Locate and identify every blood parasite.
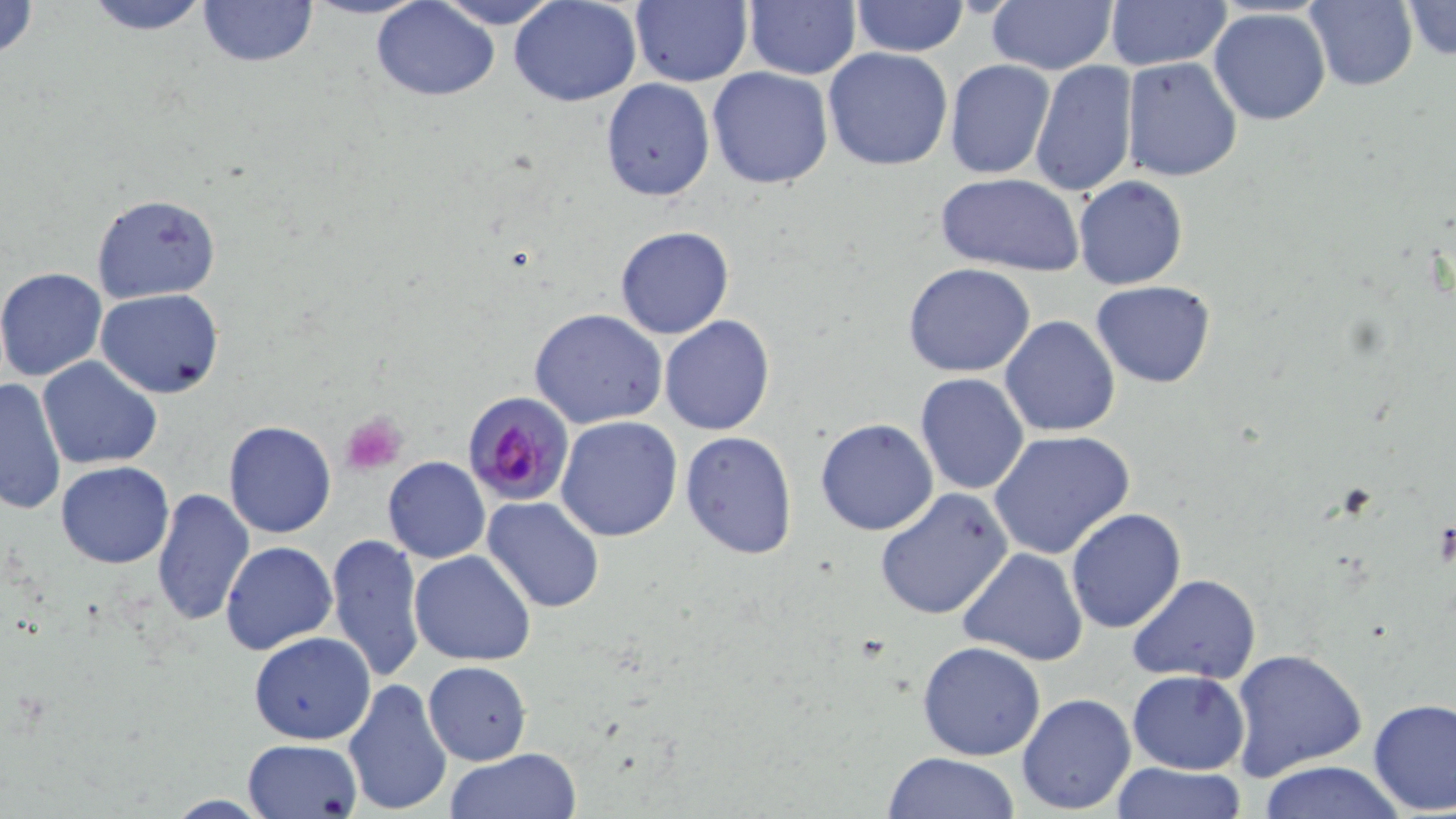

Approximate bounding boxes as named x1/y1/x2/y2 corners in pixels.
Plasmodium falciparum-infected red blood cells: (x1=464, y1=393, x2=576, y2=507).
No Plasmodium ovale, Plasmodium malariae, Plasmodium vivax, Babesia divergens, or Trypanosoma brucei observed.

Platelet locations: (x1=340, y1=411, x2=409, y2=474). Uninfected red blood cell locations: (x1=0, y1=0, x2=41, y2=65), (x1=80, y1=0, x2=215, y2=35), (x1=198, y1=0, x2=317, y2=67), (x1=302, y1=0, x2=428, y2=19), (x1=431, y1=0, x2=567, y2=29), (x1=508, y1=0, x2=643, y2=106), (x1=629, y1=0, x2=753, y2=87), (x1=743, y1=0, x2=861, y2=80), (x1=984, y1=0, x2=1119, y2=74), (x1=1302, y1=0, x2=1418, y2=91), (x1=1399, y1=0, x2=1455, y2=63), (x1=370, y1=1, x2=502, y2=101), (x1=850, y1=1, x2=969, y2=56), (x1=1103, y1=1, x2=1233, y2=71), (x1=1207, y1=8, x2=1332, y2=126), (x1=1138, y1=32, x2=1305, y2=169), (x1=823, y1=46, x2=953, y2=172), (x1=1120, y1=56, x2=1242, y2=181), (x1=945, y1=59, x2=1055, y2=179), (x1=1031, y1=61, x2=1138, y2=197), (x1=706, y1=66, x2=834, y2=190), (x1=600, y1=78, x2=716, y2=201), (x1=934, y1=173, x2=1085, y2=275), (x1=1074, y1=175, x2=1188, y2=291), (x1=90, y1=192, x2=221, y2=306), (x1=614, y1=225, x2=735, y2=341), (x1=901, y1=262, x2=1038, y2=378), (x1=0, y1=267, x2=109, y2=382), (x1=1092, y1=280, x2=1215, y2=387), (x1=95, y1=289, x2=224, y2=398), (x1=530, y1=309, x2=668, y2=429), (x1=659, y1=315, x2=775, y2=437), (x1=1000, y1=315, x2=1121, y2=438), (x1=37, y1=357, x2=163, y2=472), (x1=914, y1=372, x2=1029, y2=496), (x1=0, y1=376, x2=69, y2=515), (x1=555, y1=415, x2=684, y2=542), (x1=814, y1=419, x2=940, y2=536), (x1=223, y1=420, x2=336, y2=538), (x1=988, y1=429, x2=1134, y2=560), (x1=679, y1=431, x2=798, y2=559), (x1=383, y1=456, x2=489, y2=563), (x1=57, y1=461, x2=174, y2=567), (x1=876, y1=487, x2=1013, y2=621), (x1=152, y1=488, x2=255, y2=627), (x1=480, y1=495, x2=606, y2=615), (x1=1064, y1=506, x2=1186, y2=633), (x1=326, y1=533, x2=426, y2=684), (x1=220, y1=540, x2=338, y2=654), (x1=958, y1=547, x2=1089, y2=666), (x1=408, y1=549, x2=536, y2=666), (x1=1127, y1=574, x2=1261, y2=685), (x1=250, y1=631, x2=376, y2=744), (x1=293, y1=638, x2=436, y2=779), (x1=917, y1=639, x2=1046, y2=761), (x1=1229, y1=646, x2=1366, y2=777), (x1=424, y1=661, x2=531, y2=765), (x1=1127, y1=670, x2=1251, y2=774), (x1=342, y1=677, x2=453, y2=815), (x1=1016, y1=692, x2=1137, y2=815), (x1=1367, y1=697, x2=1455, y2=816), (x1=242, y1=737, x2=362, y2=818), (x1=444, y1=748, x2=583, y2=819), (x1=880, y1=751, x2=1023, y2=818), (x1=1110, y1=761, x2=1246, y2=817), (x1=1254, y1=761, x2=1410, y2=819). Slide-level diagnosis: Plasmodium falciparum. Image is 1456×819 pixels. Thin blood film. 1000x magnification. May-Grünwald-Giemsa stain. Single field of view. Optical microscopy.